Locate every blood parasite and identify its species.
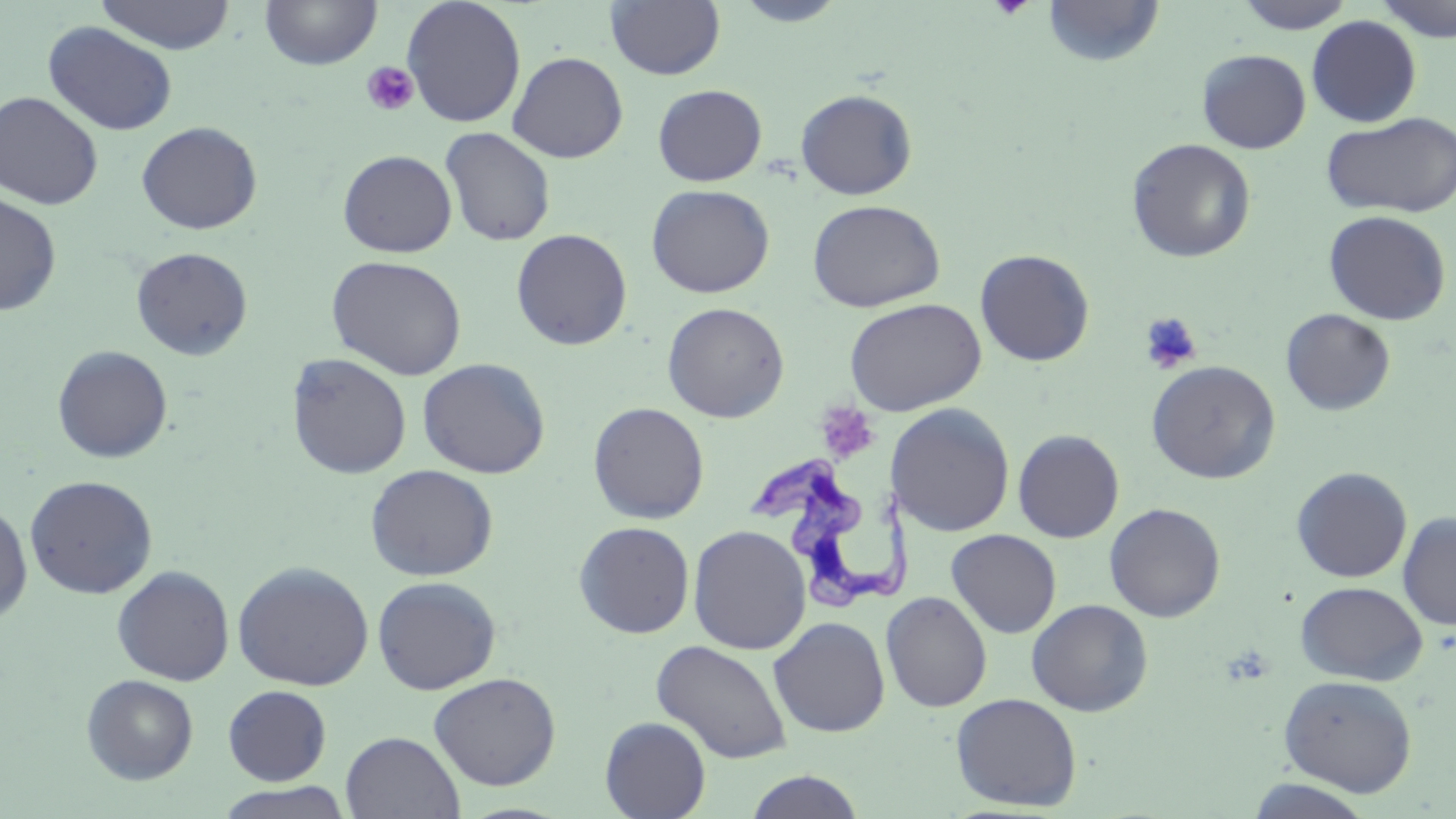
Approximate bounding boxes as [x1, y1, x2, y2] in pixels.
Trypanosoma brucei: [745, 456, 920, 610].
No Plasmodium falciparum, Plasmodium ovale, Plasmodium malariae, Plasmodium vivax, or Babesia divergens observed.

Summary:
  - Uninfected red blood cell locations: [94, 0, 236, 54], [259, 0, 382, 70], [402, 0, 526, 127], [605, 0, 726, 80], [730, 0, 851, 27], [1042, 0, 1165, 67], [1233, 0, 1357, 33], [1373, 0, 1456, 42], [1306, 15, 1422, 127], [42, 20, 178, 137], [1197, 49, 1311, 153], [508, 51, 628, 164], [652, 84, 767, 186], [795, 89, 918, 200], [0, 91, 104, 210], [1321, 112, 1456, 218], [136, 121, 262, 234], [440, 127, 555, 247], [1126, 138, 1256, 263], [337, 150, 457, 257], [646, 184, 774, 298], [0, 192, 62, 316], [807, 199, 945, 312], [1323, 210, 1451, 325], [510, 228, 633, 351], [131, 246, 253, 361], [974, 249, 1094, 366], [327, 255, 467, 380], [844, 298, 986, 415], [662, 302, 789, 423], [1281, 308, 1396, 416], [52, 345, 173, 463], [286, 352, 412, 479], [417, 357, 551, 479], [1146, 360, 1281, 484], [588, 402, 709, 524], [887, 403, 1015, 537], [1012, 429, 1124, 543], [365, 463, 499, 581], [1291, 467, 1412, 583], [24, 475, 158, 600], [0, 501, 33, 624], [1104, 502, 1226, 623], [1397, 511, 1456, 631], [573, 520, 695, 638], [688, 524, 811, 655], [946, 528, 1062, 639], [233, 560, 374, 691], [112, 565, 235, 686], [372, 576, 502, 695], [1295, 581, 1428, 685], [880, 592, 992, 712], [1026, 598, 1153, 717], [768, 616, 890, 737], [652, 640, 794, 764], [428, 672, 561, 791], [81, 674, 198, 784], [1278, 675, 1418, 796], [223, 685, 332, 785], [949, 692, 1083, 812], [599, 716, 711, 819], [340, 731, 465, 819], [743, 770, 868, 818], [1244, 779, 1377, 818], [213, 783, 355, 819]
  - Platelet locations: [989, 0, 1034, 20], [361, 61, 419, 116], [1139, 312, 1203, 374], [820, 398, 877, 457]
  - Slide-level diagnosis: Trypanosoma brucei
  - Image size: 1456×819 pixels
  - Preparation: thin blood smear
  - Stain: May-Grünwald-Giemsa
  - Modality: optical microscopy
  - Field of view: single
  - Magnification: 1000x